State which parasite is depicted.
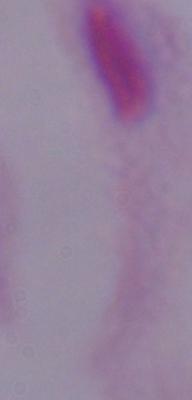
A trichomonad.

modality = photomicrograph
magnification = 1000x